Identify the parasite.
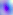
This is Toxoplasma gondii.

Summary:
  - Modality: photomicrograph
  - Magnification: 400x